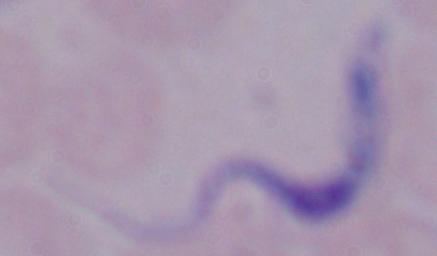

Captured at 1000x magnification. Micrograph. A trypanosome is seen.